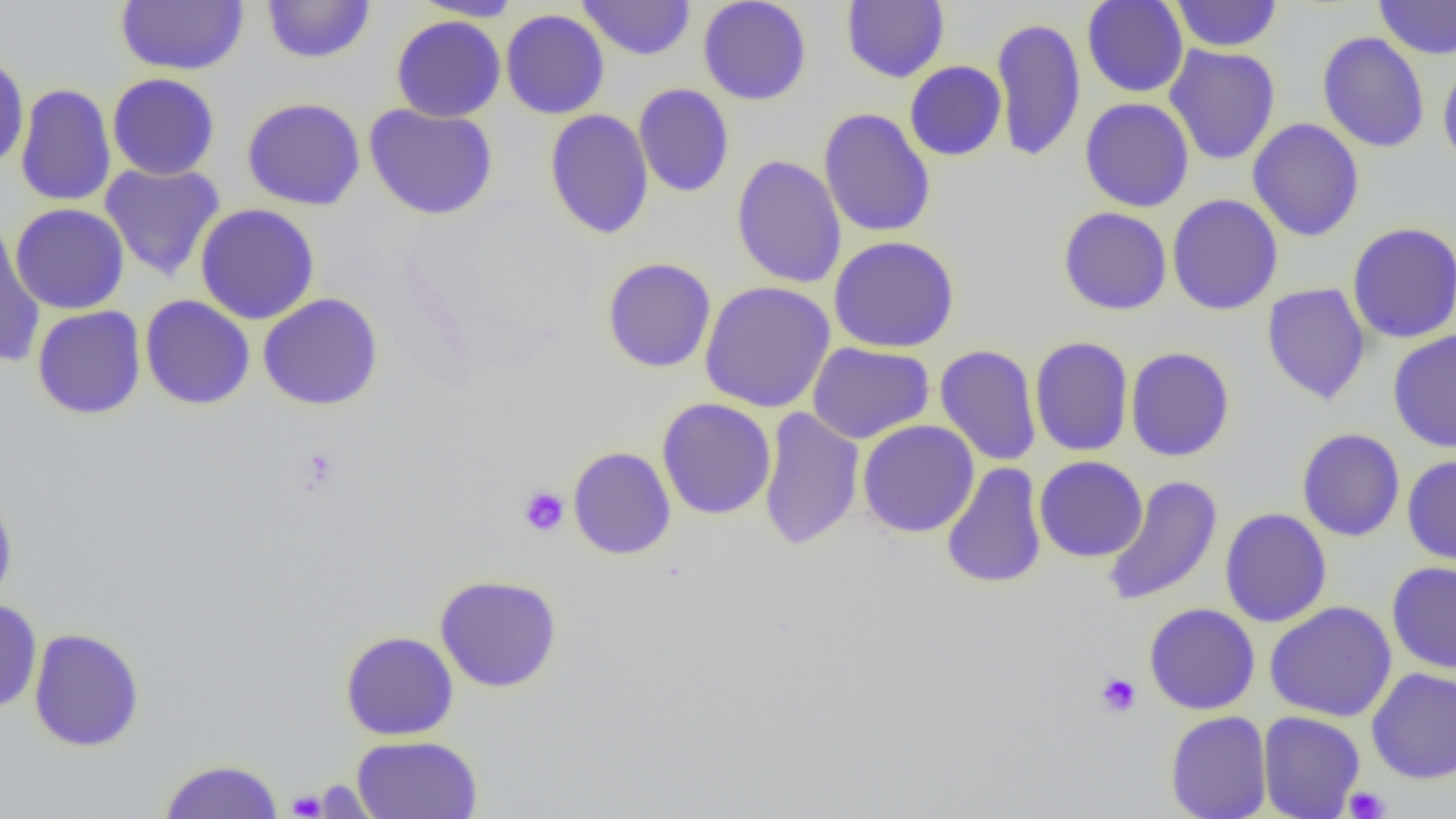
Approximate bounding boxes as [x1, y1, x2, y2] in pixels. Platelet locations: [298, 446, 340, 491], [518, 485, 570, 537], [1095, 672, 1141, 717], [1343, 786, 1390, 818], [287, 790, 327, 818]. Uninfected red blood cell locations: [261, 0, 376, 65], [411, 0, 523, 21], [578, 0, 696, 60], [698, 0, 812, 105], [1082, 0, 1188, 98], [1170, 0, 1283, 52], [1374, 0, 1456, 59], [115, 1, 248, 75], [841, 1, 949, 83], [500, 9, 610, 119], [391, 15, 506, 123], [991, 17, 1086, 162], [1317, 31, 1430, 153], [1164, 44, 1281, 165], [0, 53, 29, 170], [1437, 58, 1456, 175], [905, 61, 1007, 161], [107, 73, 220, 180], [15, 83, 116, 207], [634, 83, 734, 198], [241, 97, 366, 211], [1080, 98, 1194, 212], [363, 103, 499, 221], [818, 107, 936, 238], [544, 109, 654, 239], [1247, 118, 1364, 242], [732, 155, 847, 288], [99, 162, 226, 282], [1167, 194, 1283, 316], [10, 203, 130, 315], [195, 203, 320, 325], [1058, 207, 1172, 315], [1347, 222, 1456, 343], [0, 223, 45, 368], [828, 235, 960, 354], [602, 256, 716, 373], [699, 281, 836, 413], [1261, 282, 1372, 405], [258, 293, 384, 411], [140, 295, 255, 410], [31, 305, 147, 420], [1388, 330, 1456, 453], [1029, 336, 1133, 457], [807, 342, 935, 444], [934, 344, 1042, 467], [1125, 346, 1235, 462], [657, 398, 776, 520], [758, 405, 865, 552], [858, 420, 980, 538], [1296, 428, 1405, 542], [567, 446, 676, 560], [1402, 455, 1456, 568], [1034, 456, 1147, 562], [940, 463, 1048, 589], [1101, 475, 1223, 608], [0, 486, 18, 611], [1219, 507, 1332, 627], [1386, 561, 1456, 674], [434, 574, 563, 692], [0, 599, 42, 713], [1264, 601, 1397, 722], [1143, 602, 1260, 715], [28, 627, 145, 752], [340, 631, 459, 741], [1366, 667, 1456, 784], [1165, 710, 1272, 819], [1258, 711, 1365, 819], [351, 735, 483, 818], [157, 758, 285, 818]. Slide-level diagnosis: no evidence of blood parasites. 1000x magnification. Image is 1456×819 pixels. Single field of view. Light microscopy. Thin blood smear.